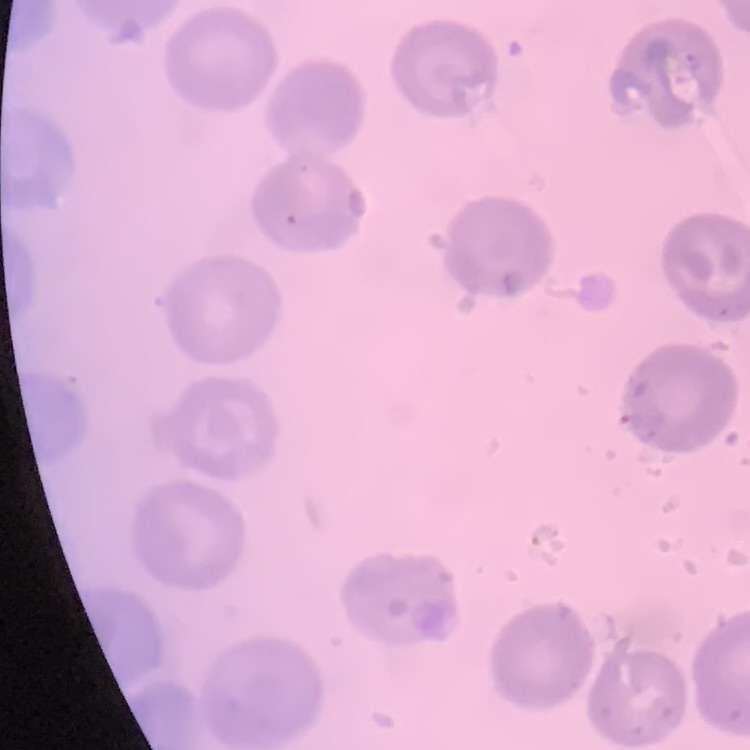

The red blood cells show no rouleaux formation. Stained with either Field's or Giemsa. Thin blood smear. One tile cut from a larger photomicrograph.